Give the extent of all Plasmodium vivax-infected red blood cells.
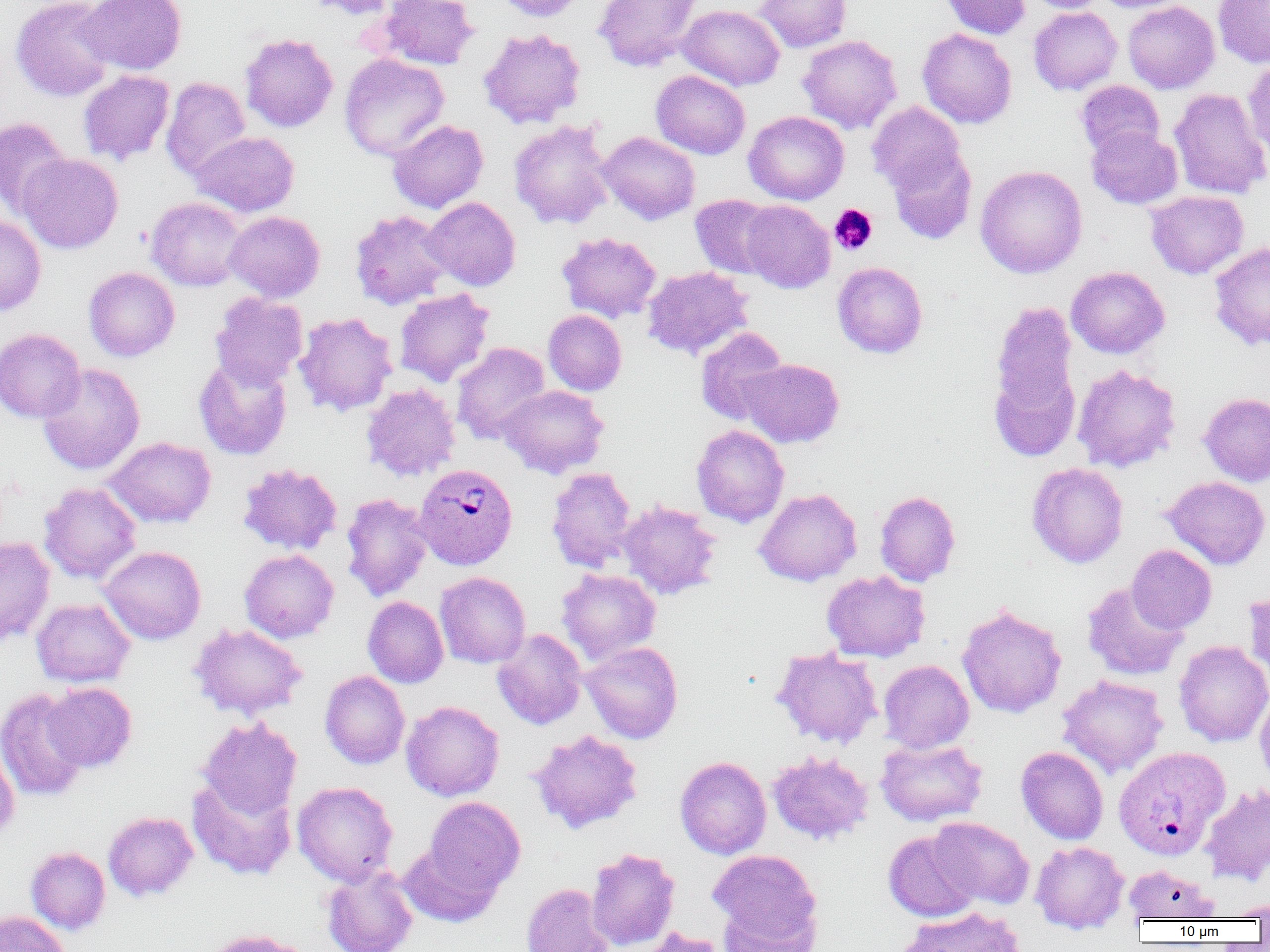

Approximate bounding boxes as (x1,y1)-(x2,y2) corner pairs in pixels.
Plasmodium vivax-infected red blood cells: (415,463)-(518,569), (1113,746)-(1230,859).

Platelet locations: (829,204)-(877,255). Uninfected red blood cell locations: (11,0)-(117,101), (80,0)-(187,75), (301,0)-(399,20), (378,0)-(479,70), (494,0)-(589,22), (593,0)-(703,72), (754,0)-(851,52), (940,0)-(1030,39), (1024,0)-(1110,13), (1093,0)-(1193,13), (1213,0)-(1270,68), (1123,1)-(1220,93), (678,4)-(785,91), (1028,7)-(1122,95), (479,28)-(585,129), (917,28)-(1017,128), (239,33)-(338,133), (798,35)-(902,133), (339,53)-(450,161), (1243,59)-(1270,161), (77,70)-(174,166), (651,70)-(751,159), (161,77)-(251,181), (1075,80)-(1165,159), (1169,87)-(1270,200), (867,101)-(967,197), (743,111)-(849,204), (0,117)-(72,220), (388,119)-(488,213), (509,119)-(615,230), (1086,126)-(1183,209), (191,131)-(299,217), (598,131)-(700,224), (887,145)-(977,244), (17,153)-(123,254), (975,165)-(1087,278), (1146,190)-(1248,278), (690,194)-(779,279), (146,197)-(247,291), (424,197)-(521,290), (740,200)-(835,293), (350,209)-(453,309), (224,211)-(325,303), (0,214)-(46,316), (557,231)-(662,323), (1209,242)-(1270,350), (832,262)-(928,358), (642,266)-(753,360), (1066,266)-(1169,358), (83,267)-(180,361), (394,289)-(495,387), (210,292)-(308,389), (986,301)-(1082,460), (543,310)-(627,396), (293,312)-(398,416), (695,327)-(789,425), (0,328)-(85,423), (451,342)-(550,444), (194,356)-(293,460), (739,358)-(845,448), (38,363)-(145,475), (1072,364)-(1181,472), (361,383)-(461,482), (498,385)-(609,478), (1199,392)-(1270,487), (691,425)-(789,527), (104,437)-(216,528), (1027,462)-(1128,568), (238,463)-(343,555), (547,467)-(638,571), (1161,476)-(1270,569), (39,482)-(141,583), (754,488)-(861,586), (875,491)-(961,586), (341,493)-(433,602), (618,501)-(722,600), (0,537)-(55,646), (1126,545)-(1216,634), (99,546)-(206,644), (240,549)-(339,642), (557,568)-(661,664), (821,570)-(930,662), (435,571)-(531,668), (1082,582)-(1188,680), (1243,592)-(1270,682), (362,596)-(449,688), (31,598)-(135,687), (956,604)-(1067,719), (189,624)-(307,719), (491,628)-(587,730), (1174,640)-(1270,747), (581,641)-(683,743), (771,646)-(883,749), (879,660)-(974,753), (320,671)-(409,769), (1058,675)-(1168,777), (42,682)-(137,772), (0,688)-(91,802), (1255,689)-(1270,791), (401,700)-(504,801), (197,717)-(302,820), (528,729)-(643,834), (875,737)-(988,827), (0,743)-(19,842), (1016,746)-(1109,844), (768,752)-(873,845), (675,756)-(771,859), (187,774)-(297,880), (292,781)-(398,885), (1200,784)-(1270,886), (422,797)-(525,899), (103,811)-(198,901), (929,817)-(1035,910), (883,830)-(981,922), (1031,841)-(1129,933), (399,842)-(502,927), (26,846)-(110,934), (586,847)-(680,950), (709,849)-(822,944), (321,864)-(418,952), (1124,864)-(1218,922), (521,884)-(612,952), (717,895)-(820,951), (1221,899)-(1270,920), (896,906)-(1026,952), (0,910)-(71,952), (632,926)-(727,952). Slide-level diagnosis: Plasmodium vivax. Image is 1270×952 pixels. Optical microscopy. Captured at 1000x magnification. Single field of view. Thin blood film.